Report the malaria status of this cell.
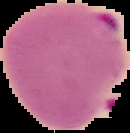
Parasitized.

Summary:
  - Image size: 130×133 pixels
  - Preparation: thin blood smear
  - Image type: segmented cell region with the area outside set to black